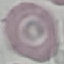

{
  "result": "no malaria parasites seen",
  "image_type": "automatically extracted cell patch, resized to 64 × 64 pixels",
  "stain": "Giemsa",
  "preparation": "thin smear",
  "capture": "smartphone through the microscope eyepiece"
}